Report the malaria status of this cell.
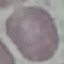

It is uninfected.

stain: Giemsa
capture: smartphone camera at the microscope eyepiece
preparation: thin blood film
image_type: automatically extracted cell patch, resized to 64 × 64 pixels